Name the parasite shown.
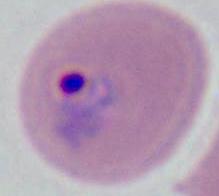
This is Plasmodium.

modality = photomicrograph
magnification = 400x or 1000x